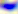

modality = micrograph
magnification = 400x
identification = Toxoplasma gondii